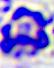
Summary:
  - Magnification: 400x
  - Identification: leukocyte
  - Modality: photomicrograph